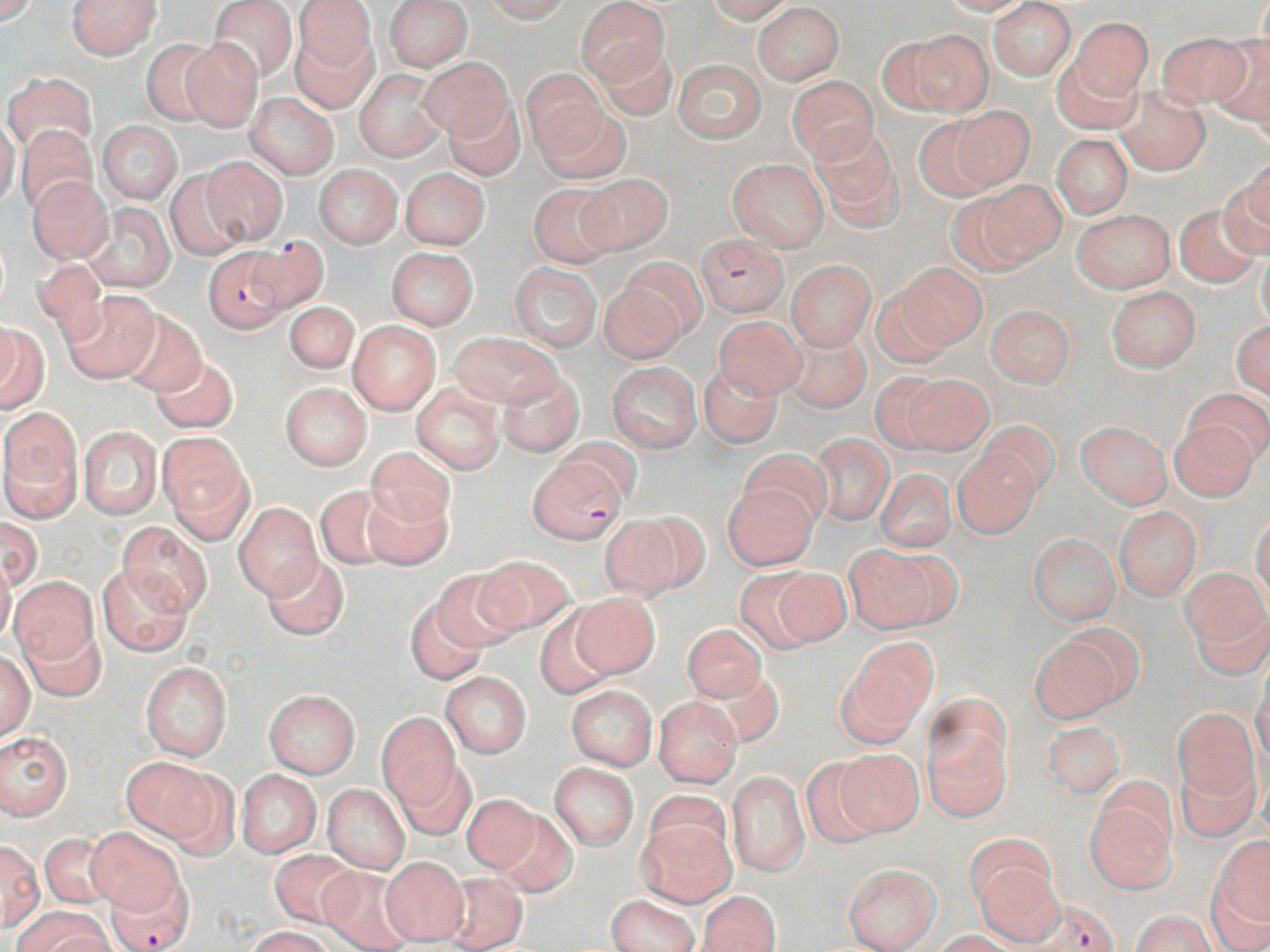

Summary:
  - Coordinate format: approximate bounding boxes as [x1, y1, x2, y2] in pixels
  - Plasmodium falciparum-infected red blood cell locations: [695, 235, 787, 318], [244, 236, 329, 315], [203, 246, 291, 331], [526, 456, 626, 546], [105, 873, 195, 952], [1020, 895, 1123, 950]
  - Uninfected red blood cell locations: [0, 0, 39, 26], [68, 0, 160, 59], [207, 0, 298, 84], [384, 0, 473, 71], [483, 0, 572, 23], [577, 0, 668, 84], [706, 0, 793, 23], [935, 1, 1037, 16], [987, 1, 1076, 81], [291, 2, 378, 98], [752, 3, 844, 85], [1069, 17, 1154, 100], [902, 29, 994, 117], [1154, 32, 1252, 110], [1207, 35, 1270, 132], [139, 39, 223, 126], [180, 40, 264, 131], [595, 42, 677, 121], [1051, 53, 1142, 134], [421, 57, 515, 142], [672, 59, 766, 142], [354, 69, 448, 161], [520, 70, 609, 157], [3, 71, 97, 154], [786, 75, 878, 164], [1115, 87, 1210, 175], [245, 92, 339, 179], [441, 97, 524, 181], [535, 100, 630, 185], [946, 105, 1037, 193], [912, 113, 1003, 202], [0, 118, 19, 210], [98, 120, 183, 203], [16, 125, 99, 214], [807, 126, 905, 232], [1051, 135, 1133, 218], [201, 156, 287, 245], [729, 158, 829, 250], [313, 164, 403, 249], [1225, 165, 1270, 253], [164, 167, 250, 261], [400, 168, 489, 249], [579, 173, 672, 254], [28, 178, 113, 263], [971, 181, 1067, 267], [527, 182, 619, 268], [947, 192, 1037, 277], [83, 202, 175, 294], [1173, 203, 1263, 286], [1070, 208, 1176, 293], [385, 247, 479, 329], [1257, 250, 1270, 328], [619, 256, 711, 342], [34, 259, 108, 345], [786, 260, 876, 350], [509, 262, 602, 353], [900, 263, 988, 350], [599, 273, 692, 363], [868, 284, 957, 368], [1106, 286, 1201, 372], [62, 290, 159, 383], [283, 301, 359, 376], [985, 304, 1076, 388], [117, 310, 206, 398], [713, 315, 806, 399], [1231, 319, 1270, 397], [348, 321, 440, 414], [0, 324, 49, 414], [783, 329, 871, 413], [449, 331, 563, 409], [151, 354, 238, 435], [606, 361, 702, 453], [698, 362, 782, 448], [498, 369, 584, 456], [897, 373, 993, 455], [280, 382, 372, 470], [411, 382, 505, 474], [1186, 389, 1270, 467], [1, 413, 82, 518], [1169, 419, 1259, 501], [1077, 420, 1172, 509], [976, 421, 1058, 502], [77, 425, 163, 520], [160, 434, 251, 537], [810, 434, 895, 524], [553, 436, 644, 509], [366, 447, 455, 530], [740, 447, 831, 531], [954, 451, 1042, 538], [875, 469, 957, 552], [721, 484, 818, 570], [315, 485, 403, 569], [363, 487, 451, 570], [234, 502, 322, 599], [1114, 506, 1202, 600], [608, 513, 702, 599], [1250, 514, 1270, 605], [0, 516, 43, 591], [116, 523, 213, 616], [1028, 533, 1121, 624], [844, 545, 948, 634], [475, 553, 578, 637], [262, 554, 349, 641], [0, 555, 15, 648], [97, 564, 191, 657], [759, 565, 851, 648], [431, 566, 524, 653], [1181, 567, 1268, 652], [8, 576, 99, 666], [569, 593, 661, 677], [404, 597, 488, 686], [1188, 598, 1270, 680], [534, 609, 616, 699], [21, 622, 106, 702], [681, 623, 770, 704], [1029, 635, 1124, 724], [838, 643, 933, 742], [0, 649, 36, 741], [141, 661, 232, 760], [706, 663, 785, 748], [441, 671, 532, 758], [1252, 671, 1270, 768], [566, 685, 658, 770], [265, 690, 360, 778], [653, 696, 742, 787], [1172, 706, 1260, 805], [377, 715, 461, 808], [922, 720, 1012, 821], [1042, 721, 1125, 799], [0, 733, 72, 819], [836, 747, 925, 835], [799, 756, 889, 849], [124, 757, 217, 844], [1176, 757, 1261, 843], [394, 759, 476, 840], [549, 762, 639, 850], [235, 769, 321, 858], [727, 771, 809, 877], [322, 784, 410, 871], [1084, 785, 1178, 893], [642, 787, 733, 872], [461, 792, 542, 874], [492, 807, 578, 896], [635, 815, 737, 907], [88, 826, 184, 916], [40, 833, 116, 909], [964, 835, 1057, 917], [1213, 836, 1270, 922], [0, 840, 44, 933], [271, 849, 359, 927], [380, 856, 469, 945], [843, 863, 941, 951], [971, 863, 1065, 945], [318, 866, 415, 951], [441, 872, 528, 951], [1205, 873, 1270, 952], [697, 891, 781, 952], [607, 894, 700, 952], [13, 905, 110, 952], [1132, 910, 1216, 952], [245, 926, 332, 952], [933, 930, 1022, 952]
  - Slide-level diagnosis: Plasmodium falciparum
  - Stain: May-Grünwald-Giemsa
  - Magnification: 1000x
  - Modality: optical microscopy
  - Field of view: one of a larger specimen
  - Preparation: thin blood film
  - Image size: 1270×952 pixels